Describe the morphology of the erythrocytes.
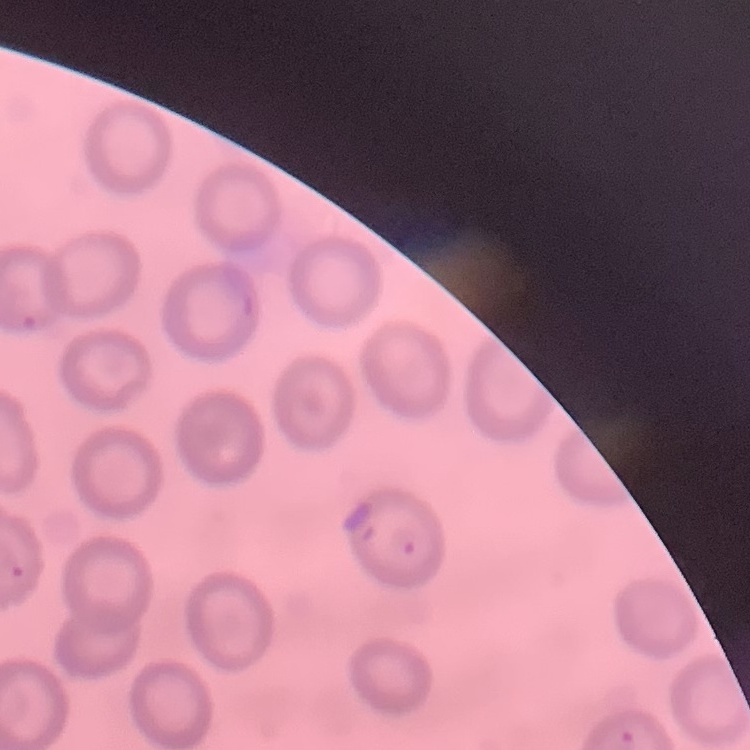
They show no rouleaux formation.

Summary:
  - Preparation: thin peripheral smear
  - Image type: one tile cut from a larger photomicrograph
  - Stain: Field's or Giemsa